Locate every blood parasite and identify its species.
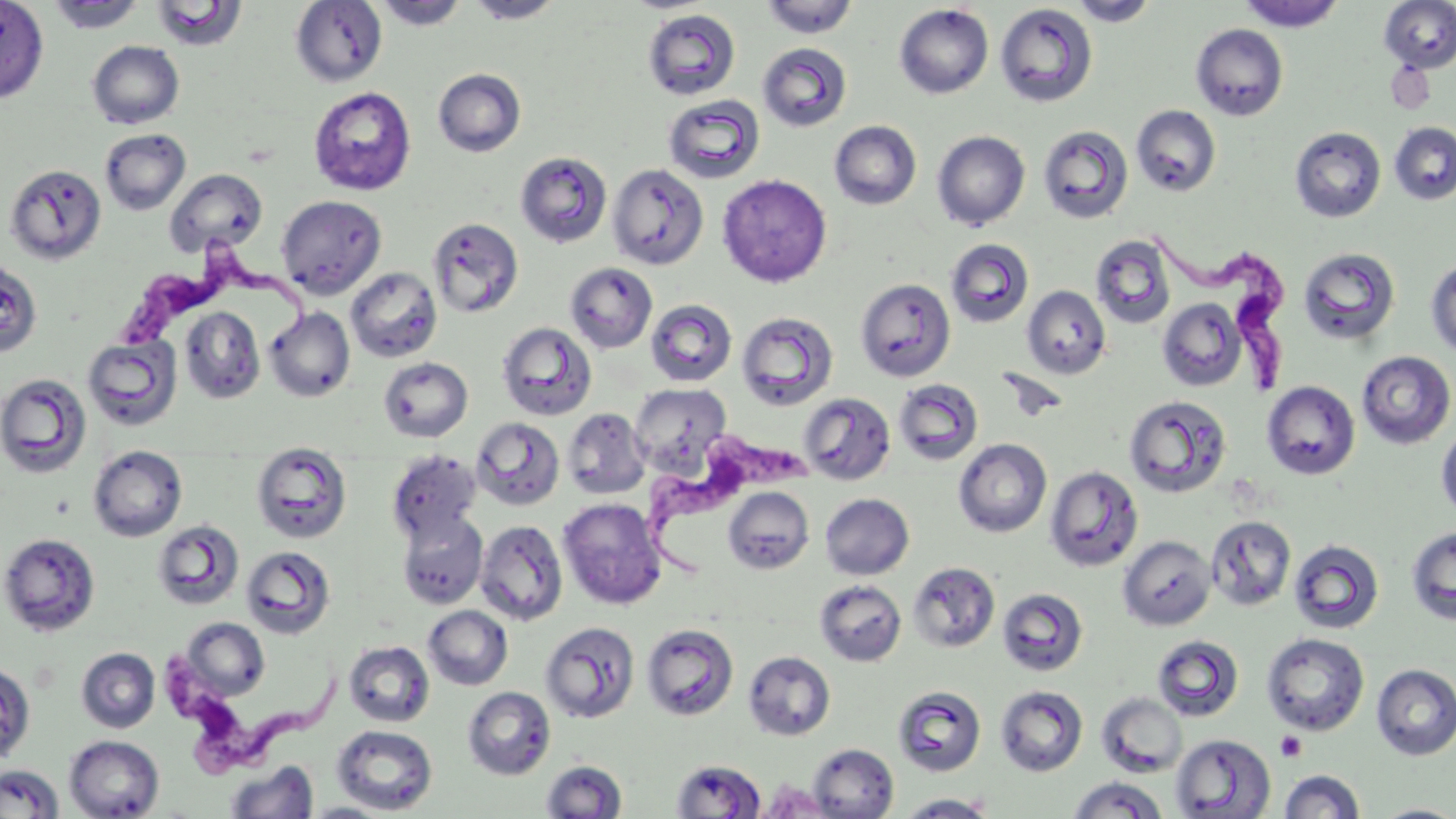

Approximate bounding boxes as (x1, y1, x2, y2) in pixels.
Trypanosoma brucei: (1142, 226, 1298, 399), (122, 237, 336, 356), (634, 427, 815, 577), (151, 648, 353, 780).
No Plasmodium falciparum, Plasmodium ovale, Plasmodium malariae, Plasmodium vivax, or Babesia divergens observed.

Summary:
  - Platelet locations (subset): (1276, 731, 1306, 761)
  - Uninfected red blood cell locations (subset): (0, 0, 49, 104), (760, 0, 859, 39), (1067, 0, 1160, 27), (1237, 0, 1346, 31), (1379, 0, 1456, 72), (46, 1, 147, 33), (151, 1, 247, 51), (290, 1, 388, 87), (370, 1, 471, 30), (463, 1, 567, 23), (894, 4, 994, 99), (994, 4, 1098, 108), (642, 9, 741, 101), (1191, 23, 1288, 121), (87, 40, 184, 129), (758, 42, 852, 132), (433, 68, 526, 157), (308, 86, 416, 196), (663, 94, 765, 184), (1131, 105, 1221, 197), (829, 120, 922, 210), (1389, 122, 1456, 205), (1037, 125, 1134, 225), (1290, 127, 1387, 223), (99, 128, 191, 215), (932, 130, 1030, 230), (514, 151, 613, 248), (4, 163, 106, 265), (607, 163, 709, 270), (165, 168, 268, 258), (717, 174, 832, 287), (276, 194, 387, 298), (428, 217, 524, 319), (1090, 235, 1177, 328), (945, 238, 1034, 327), (1298, 247, 1401, 345), (0, 258, 42, 358), (1426, 258, 1456, 358), (565, 262, 657, 353), (345, 267, 442, 363), (855, 278, 956, 382), (1022, 285, 1111, 379), (1157, 298, 1247, 391), (645, 299, 737, 387), (180, 306, 265, 404), (264, 307, 356, 402), (736, 311, 839, 411), (497, 322, 597, 421), (83, 335, 183, 431), (1357, 351, 1455, 449), (378, 357, 473, 442), (0, 373, 93, 478), (893, 379, 984, 466), (1261, 381, 1360, 480), (630, 383, 732, 474), (799, 385, 984, 472), (799, 391, 896, 486), (1123, 395, 1232, 498), (562, 407, 651, 500), (471, 417, 565, 510), (1435, 421, 1456, 521), (953, 438, 1051, 537), (251, 444, 353, 544), (88, 445, 188, 542), (386, 449, 483, 543), (1044, 465, 1143, 571), (723, 487, 815, 574), (820, 493, 914, 579), (558, 498, 667, 610), (396, 511, 488, 608), (1206, 515, 1297, 611), (152, 520, 245, 611), (475, 520, 568, 625), (1405, 525, 1456, 625), (0, 532, 101, 637), (1118, 535, 1217, 631), (1288, 538, 1384, 634), (241, 546, 336, 639), (907, 561, 1000, 652), (814, 580, 907, 666), (997, 587, 1089, 677), (423, 605, 513, 690), (181, 617, 270, 700), (541, 621, 640, 724), (641, 623, 739, 721), (1261, 633, 1370, 735), (1152, 635, 1245, 722), (344, 640, 435, 727), (76, 648, 160, 733), (743, 651, 836, 741), (0, 662, 36, 765), (1371, 663, 1456, 761), (995, 685, 1088, 776), (462, 686, 556, 780), (893, 686, 987, 777), (1096, 692, 1188, 778), (332, 725, 438, 814), (1171, 734, 1276, 818), (64, 735, 165, 818), (807, 743, 898, 819), (671, 759, 766, 818), (541, 760, 627, 818), (226, 761, 319, 818), (1, 764, 64, 819), (1279, 769, 1365, 818), (1068, 776, 1169, 818), (759, 779, 835, 817), (895, 793, 998, 818), (301, 802, 396, 818), (1371, 803, 1456, 818)
  - Slide-level diagnosis: Trypanosoma brucei
  - Image size: 1456×819 pixels
  - Preparation: thin blood film
  - Modality: light microscopy
  - Field of view: one of a larger specimen
  - Stain: May-Grünwald-Giemsa
  - Magnification: 1000x